State the preparation type.
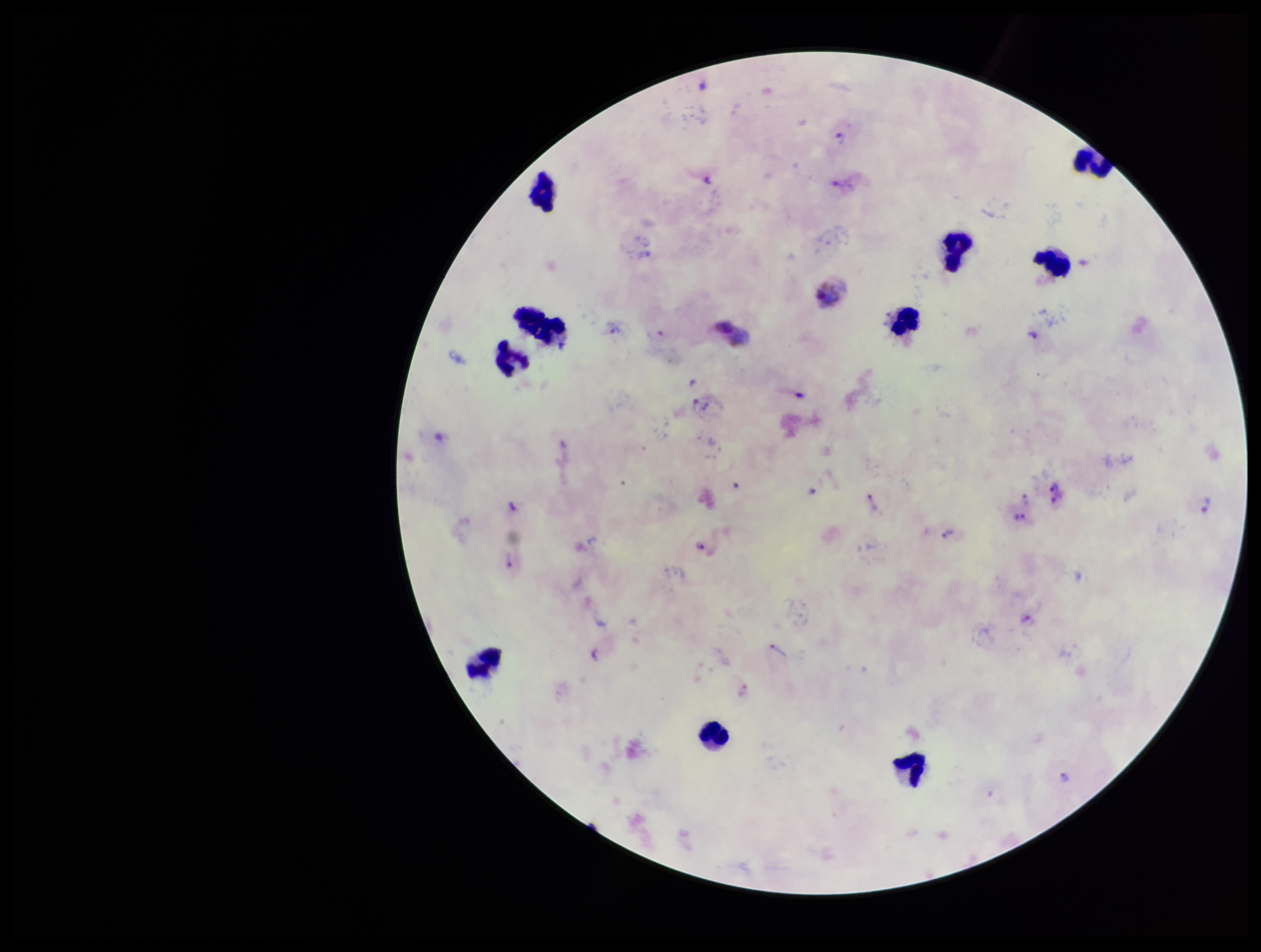

Thick.

Plasmodium parasites: detected. Giemsa stain. Species reported for this patient: Plasmodium vivax. Single field of view. Parasite count: 27. Patient malaria status: positive. Leukocyte count: 10. Photographed through the microscope eyepiece with a smartphone camera. Image is 1261×952 pixels.